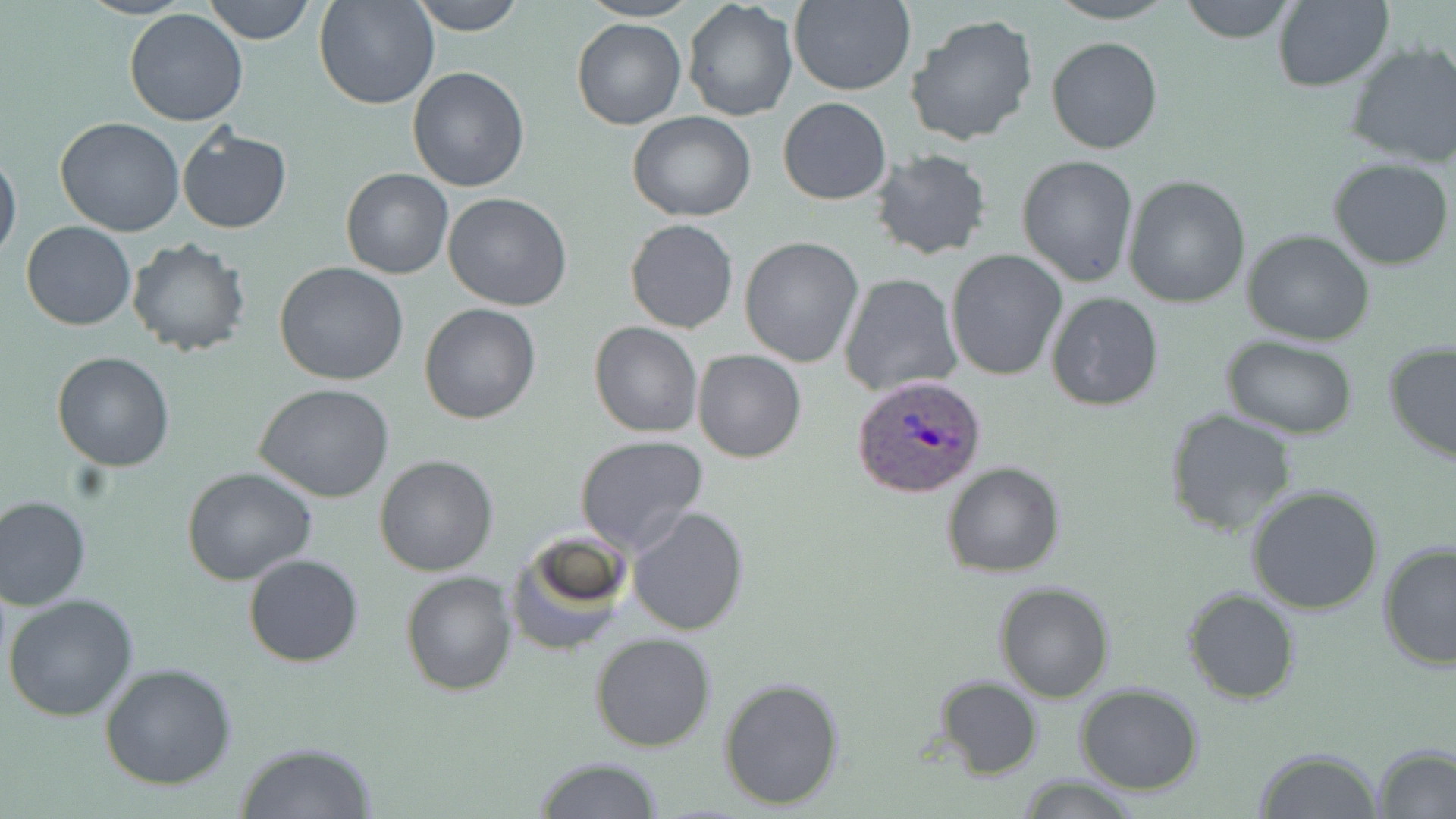
Approximate bounding boxes as [x1, y1, x2, y2] in pixels. Uninfected red blood cell locations: [76, 0, 194, 21], [201, 0, 317, 45], [313, 0, 439, 109], [409, 0, 528, 34], [579, 0, 698, 22], [789, 0, 915, 96], [1045, 0, 1179, 24], [1177, 0, 1300, 42], [682, 1, 797, 120], [1270, 1, 1394, 91], [123, 10, 247, 127], [904, 12, 1039, 147], [572, 17, 685, 130], [1045, 37, 1164, 154], [1341, 41, 1456, 170], [406, 66, 530, 192], [777, 97, 891, 205], [627, 112, 757, 222], [55, 118, 186, 238], [176, 126, 291, 234], [867, 147, 994, 262], [0, 151, 22, 265], [1017, 154, 1140, 288], [1329, 159, 1454, 270], [340, 167, 453, 279], [1123, 174, 1252, 307], [443, 192, 573, 311], [625, 219, 739, 333], [20, 221, 136, 331], [1242, 229, 1375, 345], [739, 235, 863, 368], [126, 237, 252, 356], [945, 250, 1067, 380], [274, 262, 409, 386], [838, 273, 962, 397], [1044, 292, 1165, 410], [418, 303, 541, 424], [588, 320, 703, 438], [1223, 336, 1358, 438], [1382, 341, 1456, 465], [693, 349, 806, 463], [52, 352, 174, 472], [254, 384, 396, 503], [1164, 408, 1299, 536], [575, 436, 709, 554], [373, 455, 499, 576], [940, 461, 1065, 578], [181, 466, 318, 586], [1246, 486, 1386, 614], [3, 494, 108, 713], [0, 496, 91, 610], [626, 504, 748, 636], [506, 532, 632, 655], [1376, 540, 1456, 669], [243, 553, 364, 667], [400, 570, 518, 695], [993, 581, 1114, 702], [1184, 588, 1299, 704], [3, 593, 139, 721], [589, 634, 716, 753], [100, 662, 238, 790], [934, 675, 1044, 780], [718, 676, 847, 811], [1076, 683, 1206, 796], [235, 742, 378, 819], [1373, 744, 1456, 818], [1253, 747, 1382, 819], [532, 758, 667, 818], [1016, 777, 1142, 816]. Plasmodium ovale-infected red blood cell locations: [853, 374, 988, 498]. Slide-level diagnosis: Plasmodium ovale. Light microscopy. Thin blood smear. 1000x magnification. Single field of view. May-Grünwald-Giemsa stain. Image is 1456×819 pixels.